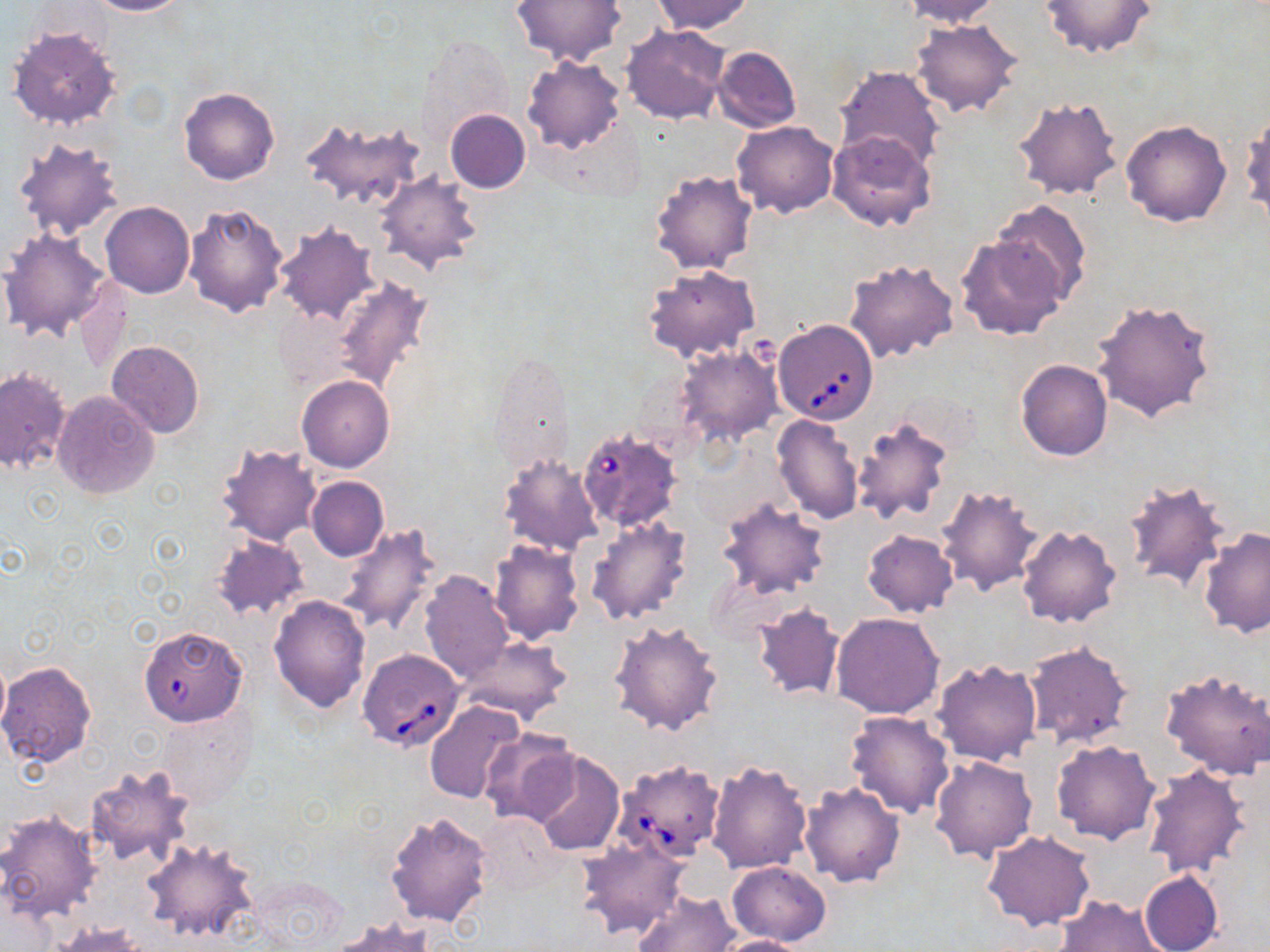

slide-level diagnosis = Babesia divergens
modality = optical microscopy
magnification = 1000x
image size = 1270×952 pixels
preparation = thin blood film
Babesia divergens-infected red blood cell locations = approximate bounding boxes as (x1, y1, x2, y2) in pixels: (774, 319, 879, 425), (578, 432, 682, 533), (138, 626, 247, 725), (357, 649, 465, 752), (612, 758, 725, 863)
stain = May-Grünwald-Giemsa
field of view = single
uninfected red blood cell locations = approximate bounding boxes as (x1, y1, x2, y2) in pixels: (83, 0, 189, 16), (511, 0, 623, 67), (651, 0, 754, 35), (897, 0, 1001, 26), (1039, 0, 1157, 59), (910, 18, 1024, 119), (621, 24, 730, 124), (7, 25, 121, 131), (419, 36, 517, 144), (712, 46, 802, 133), (522, 56, 626, 155), (833, 64, 946, 174), (179, 86, 280, 186), (1010, 95, 1124, 202), (445, 110, 530, 193), (1241, 112, 1269, 228), (297, 115, 427, 211), (1121, 119, 1231, 227), (732, 120, 838, 219), (827, 130, 937, 232), (11, 136, 122, 241), (649, 170, 757, 275), (377, 171, 481, 274), (992, 199, 1092, 304), (183, 201, 290, 318), (101, 202, 194, 298), (273, 221, 378, 326), (0, 228, 111, 341), (957, 233, 1067, 341), (843, 257, 957, 365), (644, 264, 761, 362), (332, 275, 433, 393), (1091, 297, 1218, 422), (106, 341, 204, 439), (674, 344, 781, 447), (1015, 360, 1112, 461), (0, 367, 71, 475), (297, 375, 394, 472), (51, 389, 160, 499), (771, 415, 864, 525), (851, 416, 954, 526), (216, 444, 323, 546), (496, 450, 603, 556), (306, 477, 389, 562), (1121, 478, 1231, 594), (935, 483, 1045, 594), (716, 496, 829, 600), (585, 516, 693, 625), (339, 524, 441, 638), (1016, 524, 1122, 628), (1198, 526, 1269, 640), (862, 529, 958, 617), (211, 534, 309, 621), (488, 541, 583, 644), (419, 570, 515, 683), (270, 595, 371, 713), (752, 603, 844, 701), (830, 611, 945, 719), (608, 619, 724, 736), (458, 634, 572, 723), (1022, 638, 1133, 748), (0, 652, 9, 736), (931, 658, 1042, 767), (0, 661, 97, 767), (1159, 665, 1270, 779), (424, 701, 526, 804), (156, 706, 256, 807), (845, 710, 956, 819), (479, 729, 580, 824), (1052, 738, 1160, 844), (528, 749, 625, 856), (930, 755, 1037, 862), (706, 758, 813, 874), (1142, 765, 1252, 879), (86, 766, 194, 868), (799, 780, 905, 888), (0, 810, 102, 920), (386, 810, 494, 928), (476, 813, 565, 896), (981, 830, 1097, 930), (140, 837, 261, 943), (576, 838, 689, 940), (727, 862, 830, 946), (1138, 869, 1223, 952), (632, 889, 740, 951), (1055, 894, 1167, 952), (327, 916, 438, 951), (51, 922, 145, 951), (715, 935, 812, 952)